Locate every blood parasite and identify its species.
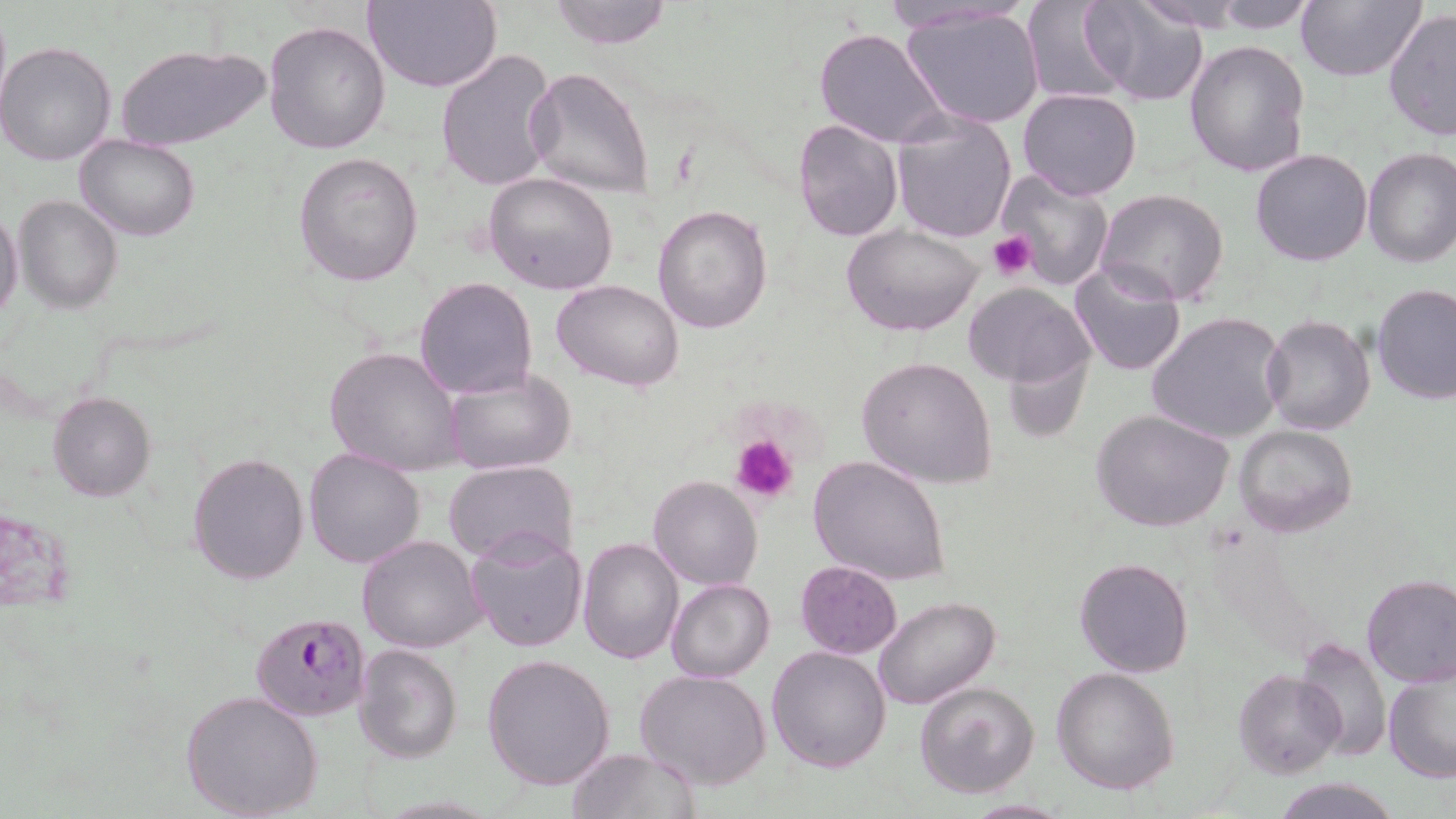

Approximate bounding boxes as (x1,y1)-(x2,y2) corner pairs in pixels.
Plasmodium falciparum-infected red blood cells: (250,611)-(370,724).
No Plasmodium ovale, Plasmodium malariae, Plasmodium vivax, Babesia divergens, or Trypanosoma brucei observed.

Platelet locations: (987,231)-(1037,279), (731,435)-(799,505). Uninfected red blood cell locations: (364,0)-(500,94), (548,0)-(673,49), (878,0)-(1035,35), (1020,0)-(1131,104), (1083,0)-(1211,105), (1129,0)-(1249,32), (1207,0)-(1324,32), (1295,0)-(1424,83), (899,6)-(1047,132), (1383,7)-(1455,143), (263,20)-(390,155), (813,27)-(950,148), (1183,38)-(1311,177), (0,41)-(118,166), (115,42)-(269,153), (435,49)-(559,193), (526,67)-(654,198), (1017,88)-(1143,201), (890,109)-(1018,246), (793,118)-(903,242), (74,134)-(200,239), (1361,146)-(1456,268), (1250,147)-(1373,266), (293,151)-(423,288), (1000,168)-(1116,289), (485,171)-(619,295), (1094,188)-(1230,307), (15,195)-(122,313), (653,203)-(774,334), (0,206)-(24,325), (839,221)-(985,337), (1068,260)-(1188,377), (414,277)-(538,400), (552,279)-(685,392), (964,283)-(1093,389), (1372,283)-(1456,404), (1148,312)-(1287,444), (1262,316)-(1376,436), (1000,338)-(1095,444), (324,347)-(464,476), (857,356)-(997,489), (445,366)-(577,475), (48,391)-(156,502), (1091,408)-(1235,533), (1234,424)-(1358,537), (304,447)-(427,569), (187,452)-(309,586), (807,455)-(952,589), (445,460)-(578,567), (647,474)-(761,590), (464,529)-(588,653), (357,534)-(488,654), (577,536)-(683,663), (1073,557)-(1194,678), (795,560)-(903,659), (1360,575)-(1456,689), (666,579)-(775,682), (873,596)-(1001,709), (1297,636)-(1391,762), (353,643)-(463,765), (767,646)-(893,772), (482,654)-(615,792), (1052,666)-(1180,795), (1383,667)-(1456,782), (1233,668)-(1346,778), (635,670)-(771,791), (914,679)-(1041,799), (181,691)-(324,819), (568,748)-(699,818), (1273,777)-(1399,818), (958,799)-(1072,817). Slide-level diagnosis: Plasmodium falciparum. May-Grünwald-Giemsa-stained preparation. Captured at 1000x magnification. Single field of view. Optical microscopy. Image is 1456×819 pixels. Thin blood film.